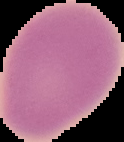
Summary:
  - Preparation: thin blood film
  - Image size: 124×142 pixels
  - Image type: cell region segmented out of the field of view; surrounding area masked to black
  - Malaria status: uninfected